Locate every Trypanosoma brucei.
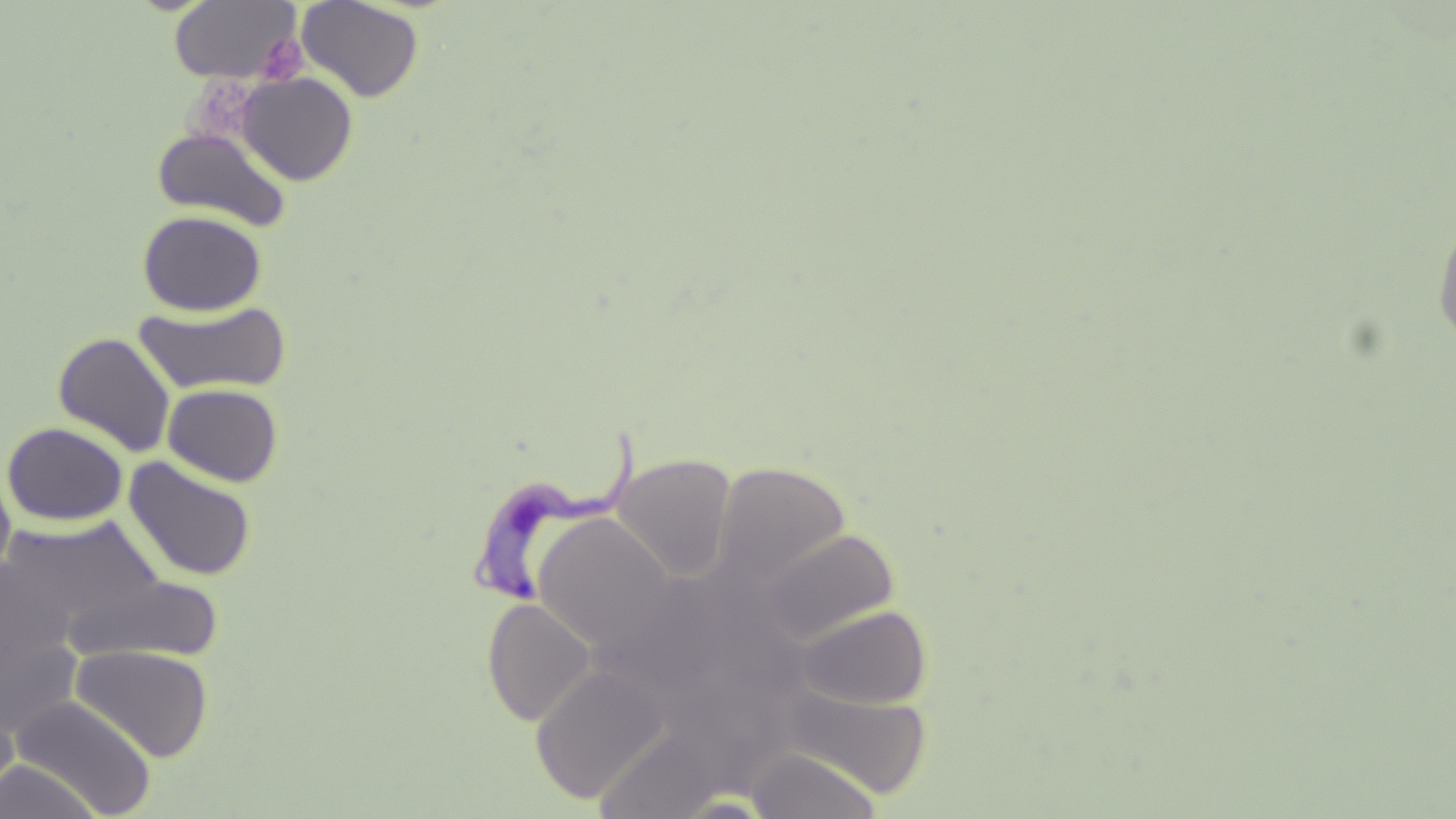

Approximate bounding boxes as [x1, y1, x2, y2] in pixels.
Trypanosoma brucei: [467, 421, 643, 603].

Uninfected red blood cell locations: [296, 0, 424, 103], [169, 1, 302, 83], [236, 72, 358, 186], [151, 126, 292, 231], [137, 210, 267, 316], [1432, 214, 1456, 349], [134, 300, 292, 395], [52, 331, 177, 456], [163, 383, 283, 486], [1, 421, 129, 526], [611, 453, 737, 583], [123, 457, 257, 582], [712, 460, 851, 591], [0, 465, 16, 584], [3, 514, 164, 637], [533, 514, 675, 653], [756, 528, 900, 646], [0, 560, 76, 677], [62, 574, 225, 663], [481, 598, 596, 726], [796, 604, 932, 710], [0, 628, 83, 739], [71, 645, 213, 762], [531, 665, 669, 804], [778, 682, 933, 799], [10, 695, 158, 818], [746, 747, 882, 818], [0, 760, 103, 819]. Platelet locations: [257, 35, 308, 83]. Slide-level diagnosis: Trypanosoma brucei. May-Grünwald-Giemsa stain. Optical microscopy. Single field of view. Image is 1456×819 pixels. 1000x magnification. Thin blood smear.